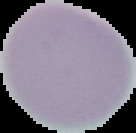 Result: no malaria parasites detected. Image is 136×133 pixels. From a thin blood film. Cell region segmented out of the field of view; the surrounding area is masked to black.